Describe the morphology of the erythrocytes.
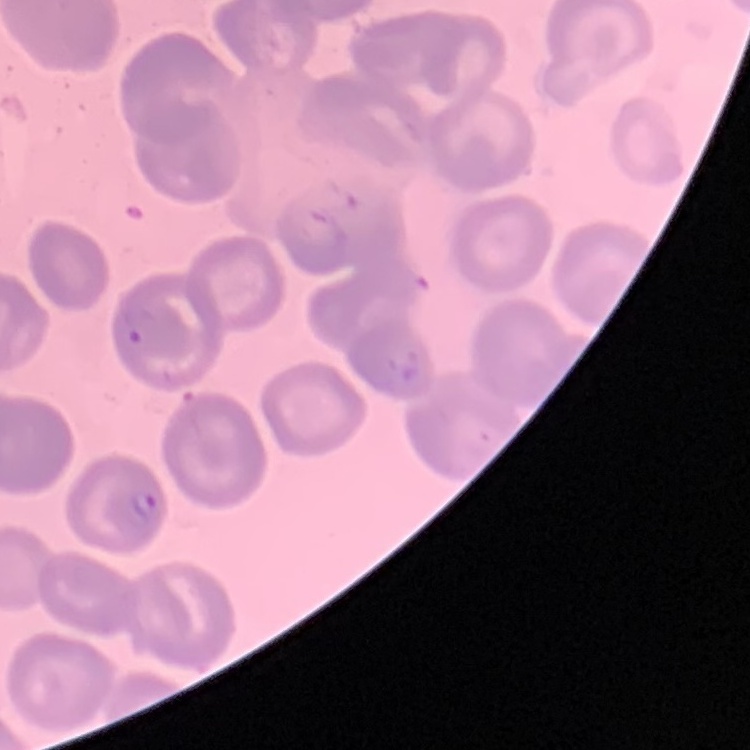
No rouleaux formation.

Summary:
  - Stain: Field's or Giemsa
  - Image type: one tile cut from a larger photomicrograph
  - Preparation: thin peripheral smear